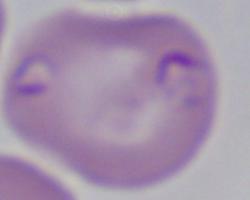

1000x magnification. Photomicrograph. A Babesia parasite is seen.